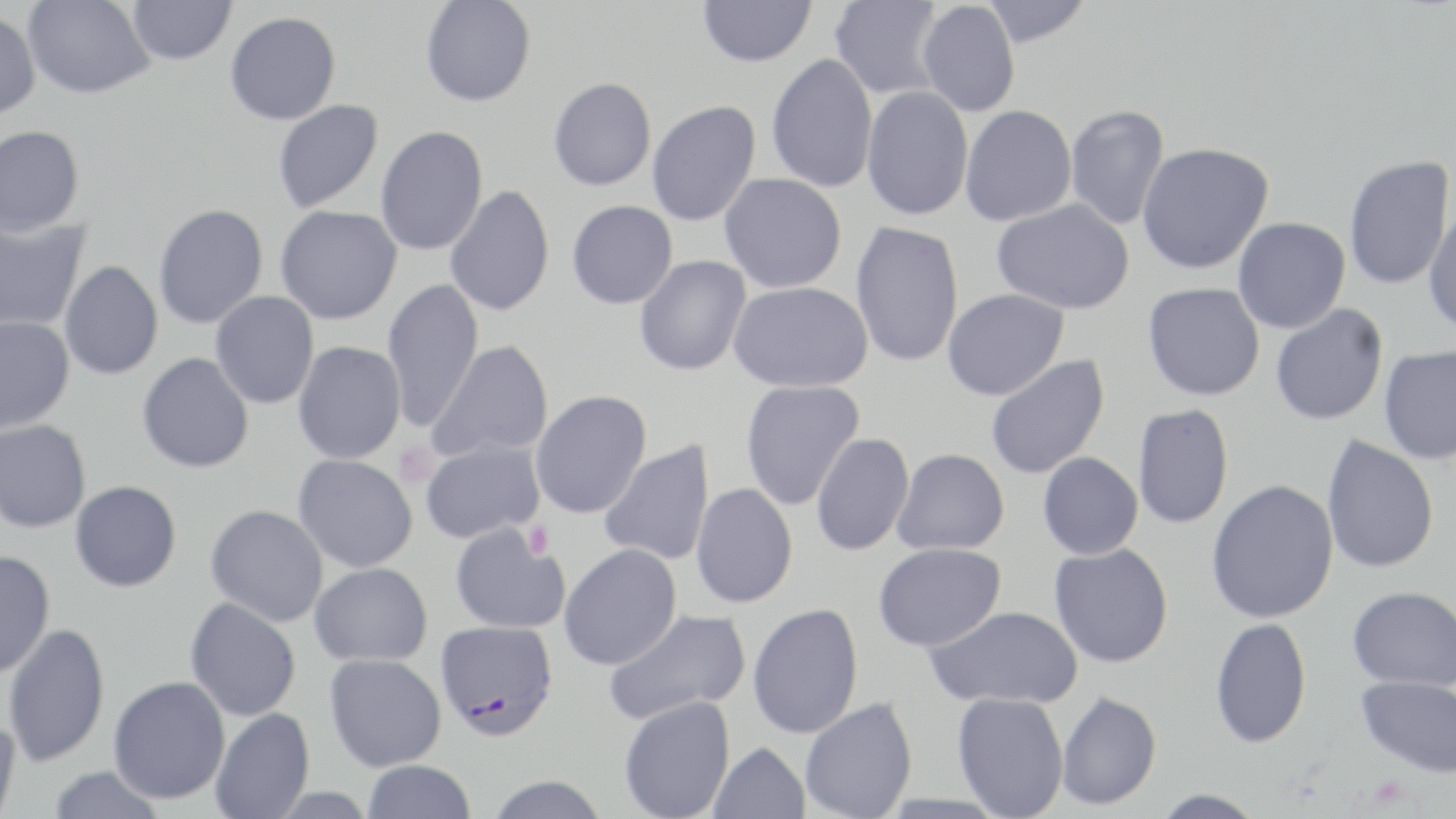
slide_level_diagnosis: Plasmodium falciparum
image_size: 1456×819 pixels
uninfected_red_blood_cell_locations: 'approximate bounding boxes as named x1/y1/x2/y2 corners in pixels: (x1=23, y1=0, x2=155, y2=99), (x1=420, y1=0, x2=536, y2=107), (x1=697, y1=0, x2=816, y2=67), (x1=829, y1=0, x2=946, y2=100), (x1=979, y1=0, x2=1093, y2=47), (x1=127, y1=1, x2=236, y2=66), (x1=916, y1=1, x2=1020, y2=117), (x1=0, y1=11, x2=41, y2=121), (x1=225, y1=11, x2=341, y2=125), (x1=766, y1=53, x2=878, y2=193), (x1=548, y1=77, x2=656, y2=191), (x1=861, y1=86, x2=973, y2=221), (x1=272, y1=99, x2=384, y2=214), (x1=646, y1=100, x2=760, y2=227), (x1=960, y1=105, x2=1077, y2=226), (x1=1065, y1=105, x2=1170, y2=231), (x1=0, y1=125, x2=85, y2=237), (x1=375, y1=125, x2=488, y2=256), (x1=1136, y1=141, x2=1274, y2=274), (x1=1343, y1=155, x2=1454, y2=291), (x1=719, y1=174, x2=847, y2=293), (x1=445, y1=184, x2=555, y2=317), (x1=567, y1=199, x2=678, y2=309), (x1=992, y1=199, x2=1135, y2=314), (x1=153, y1=203, x2=268, y2=329), (x1=275, y1=205, x2=402, y2=324), (x1=1423, y1=205, x2=1456, y2=337), (x1=0, y1=215, x2=92, y2=333), (x1=1233, y1=217, x2=1350, y2=334), (x1=850, y1=220, x2=965, y2=368), (x1=633, y1=255, x2=752, y2=376), (x1=59, y1=261, x2=163, y2=380), (x1=381, y1=277, x2=484, y2=433), (x1=728, y1=282, x2=872, y2=393), (x1=1143, y1=282, x2=1266, y2=401), (x1=943, y1=289, x2=1069, y2=400), (x1=210, y1=291, x2=319, y2=409), (x1=1270, y1=303, x2=1388, y2=426), (x1=0, y1=315, x2=75, y2=432), (x1=293, y1=340, x2=406, y2=465), (x1=427, y1=340, x2=554, y2=463), (x1=1378, y1=346, x2=1456, y2=465), (x1=137, y1=352, x2=254, y2=473), (x1=985, y1=354, x2=1110, y2=480), (x1=739, y1=380, x2=865, y2=510), (x1=529, y1=390, x2=652, y2=519), (x1=1132, y1=404, x2=1234, y2=529), (x1=0, y1=419, x2=92, y2=533), (x1=811, y1=433, x2=915, y2=556), (x1=1321, y1=434, x2=1440, y2=574), (x1=419, y1=438, x2=545, y2=544), (x1=599, y1=440, x2=715, y2=567), (x1=892, y1=448, x2=1009, y2=555), (x1=1037, y1=452, x2=1144, y2=560), (x1=293, y1=454, x2=419, y2=572), (x1=1205, y1=479, x2=1340, y2=624), (x1=70, y1=480, x2=182, y2=592), (x1=690, y1=483, x2=798, y2=609), (x1=205, y1=504, x2=328, y2=627), (x1=450, y1=524, x2=570, y2=634), (x1=873, y1=542, x2=1007, y2=651), (x1=558, y1=543, x2=682, y2=670), (x1=1049, y1=543, x2=1174, y2=668), (x1=0, y1=550, x2=55, y2=678), (x1=309, y1=563, x2=433, y2=666), (x1=1347, y1=586, x2=1456, y2=691), (x1=185, y1=596, x2=301, y2=721), (x1=747, y1=603, x2=864, y2=739), (x1=924, y1=605, x2=1083, y2=709), (x1=604, y1=609, x2=751, y2=726), (x1=1209, y1=617, x2=1312, y2=748), (x1=3, y1=622, x2=110, y2=768), (x1=324, y1=653, x2=446, y2=771), (x1=1355, y1=675, x2=1456, y2=777), (x1=108, y1=677, x2=231, y2=805), (x1=1056, y1=691, x2=1162, y2=811), (x1=952, y1=692, x2=1069, y2=818), (x1=619, y1=696, x2=735, y2=819), (x1=800, y1=697, x2=917, y2=819), (x1=210, y1=707, x2=314, y2=819), (x1=0, y1=716, x2=23, y2=819), (x1=709, y1=741, x2=810, y2=819), (x1=362, y1=760, x2=476, y2=818), (x1=47, y1=766, x2=165, y2=818), (x1=484, y1=775, x2=610, y2=819), (x1=1148, y1=789, x2=1268, y2=818)'
modality: light microscopy
platelet_locations: 'approximate bounding boxes as named x1/y1/x2/y2 corners in pixels: (x1=394, y1=441, x2=439, y2=488), (x1=522, y1=520, x2=554, y2=560)'
stain: May-Grünwald-Giemsa
field_of_view: single
preparation: thin blood smear
magnification: 1000x
plasmodium_falciparum_infected_red_blood_cell_locations: 'approximate bounding boxes as named x1/y1/x2/y2 corners in pixels: (x1=435, y1=619, x2=559, y2=741)'